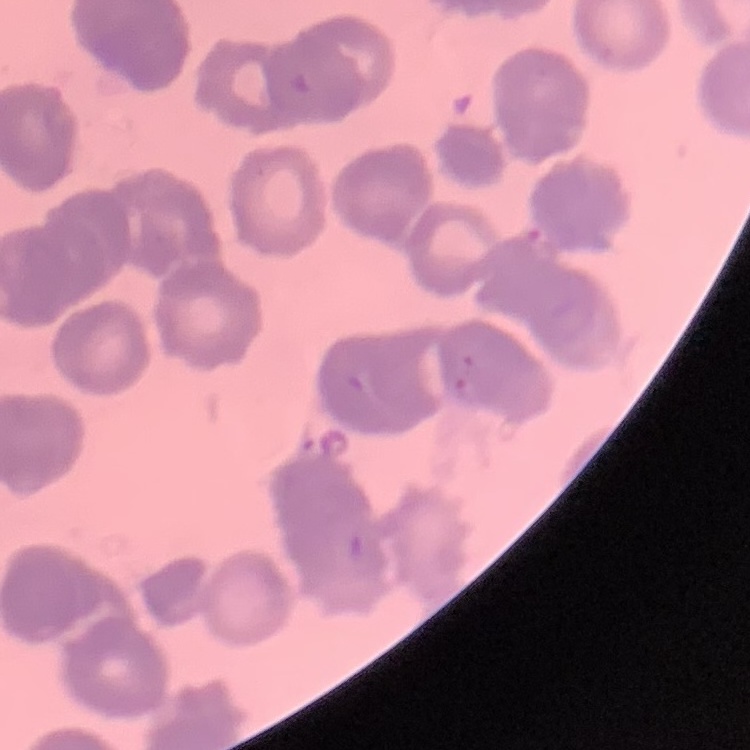

The erythrocytes exhibit rouleaux formation. Thin blood smear. Square crop of a larger photomicrograph. Field's or Giemsa stain.